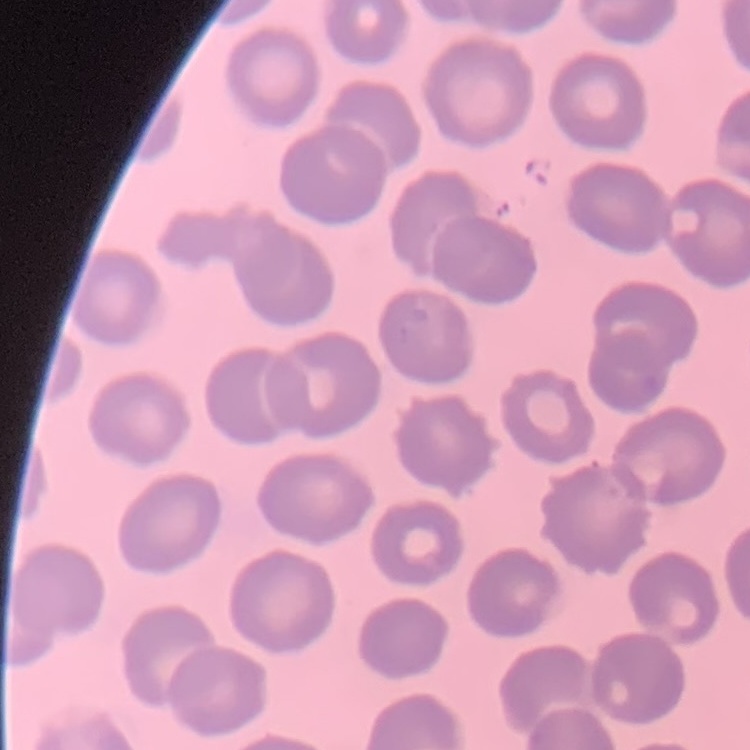
Summary:
  - Red blood cell morphology: no rouleaux formation
  - Stain: Field's or Giemsa
  - Image type: one tile cut from a larger photomicrograph
  - Preparation: thin blood film